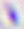 Micrograph. Captured at 400x magnification. Toxoplasma gondii is seen.